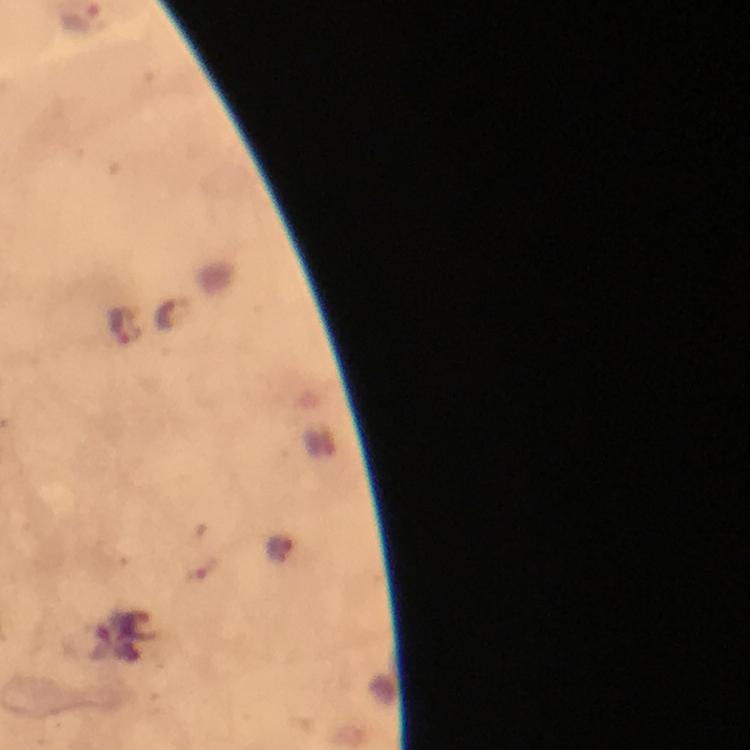 Approximate object centers, in pixels from the top-left corner. Malaria parasite locations: (x=172, y=315), (x=122, y=326). Immersion oil was used. Cropped region of a single field of view. Thick blood smear. From a malaria diagnostic workup. Image is 750×750 pixels. Giemsa-stained preparation. At 100x magnification. Photographed with a smartphone mounted on the microscope.